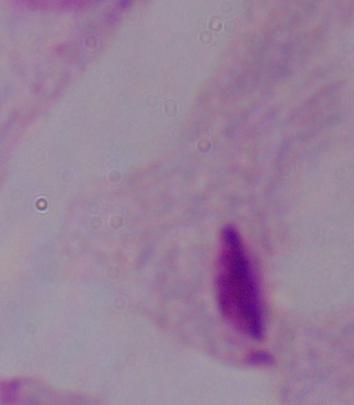
Summary:
  - Modality: photomicrograph
  - Magnification: 1000x
  - Identification: trichomonad